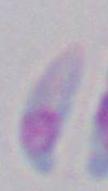

identification = Toxoplasma gondii
magnification = 1000x
modality = micrograph